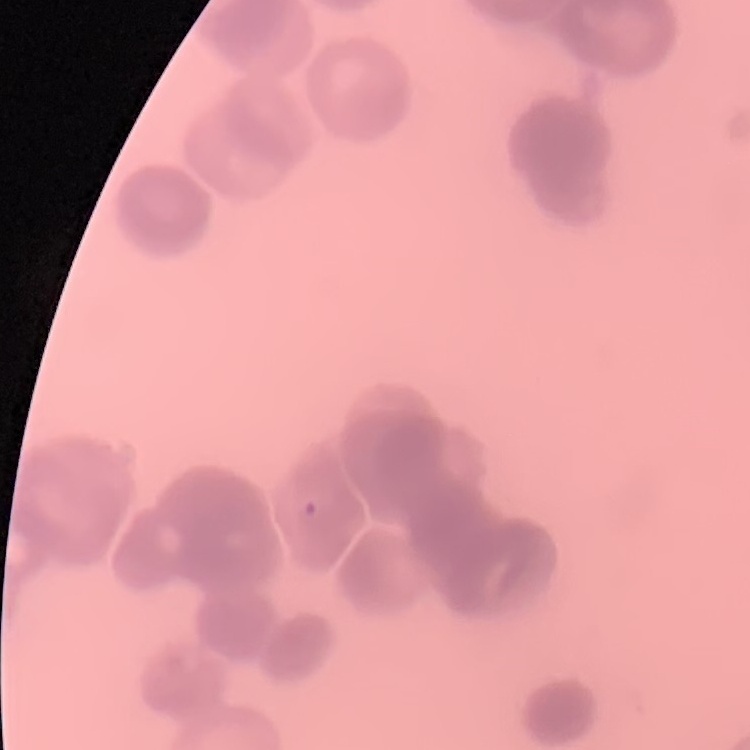

red blood cell morphology = rouleaux formation
image type = square crop of a larger photomicrograph
preparation = thin blood smear
stain = Field's or Giemsa